Report the malaria status of this cell.
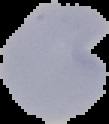

Uninfected.

{
  "image_size": "109×124 pixels",
  "image_type": "segmented cell region with the area outside set to black",
  "preparation": "thin blood film"
}